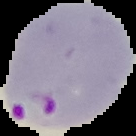
preparation = thin blood smear
image size = 136×136 pixels
malaria status = parasitized
image type = segmented cell region on a black background